Give the position of every malaria parasite.
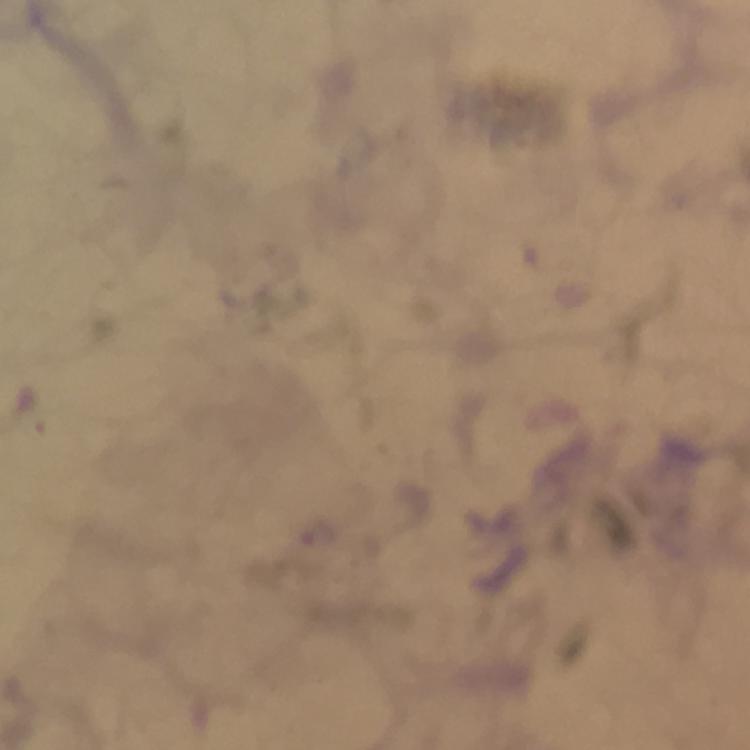
Approximate centers as (x, y) in pixels.
Malaria parasites: (320, 533).

From a diagnostic examination for malaria. Thick smear. Giemsa-stained preparation. Image is 750×750 pixels. A crop from one field of view. Immersion oil was used. Photographed through the microscope with a smartphone camera. At 100x magnification.